Outline each blood parasite and name the species.
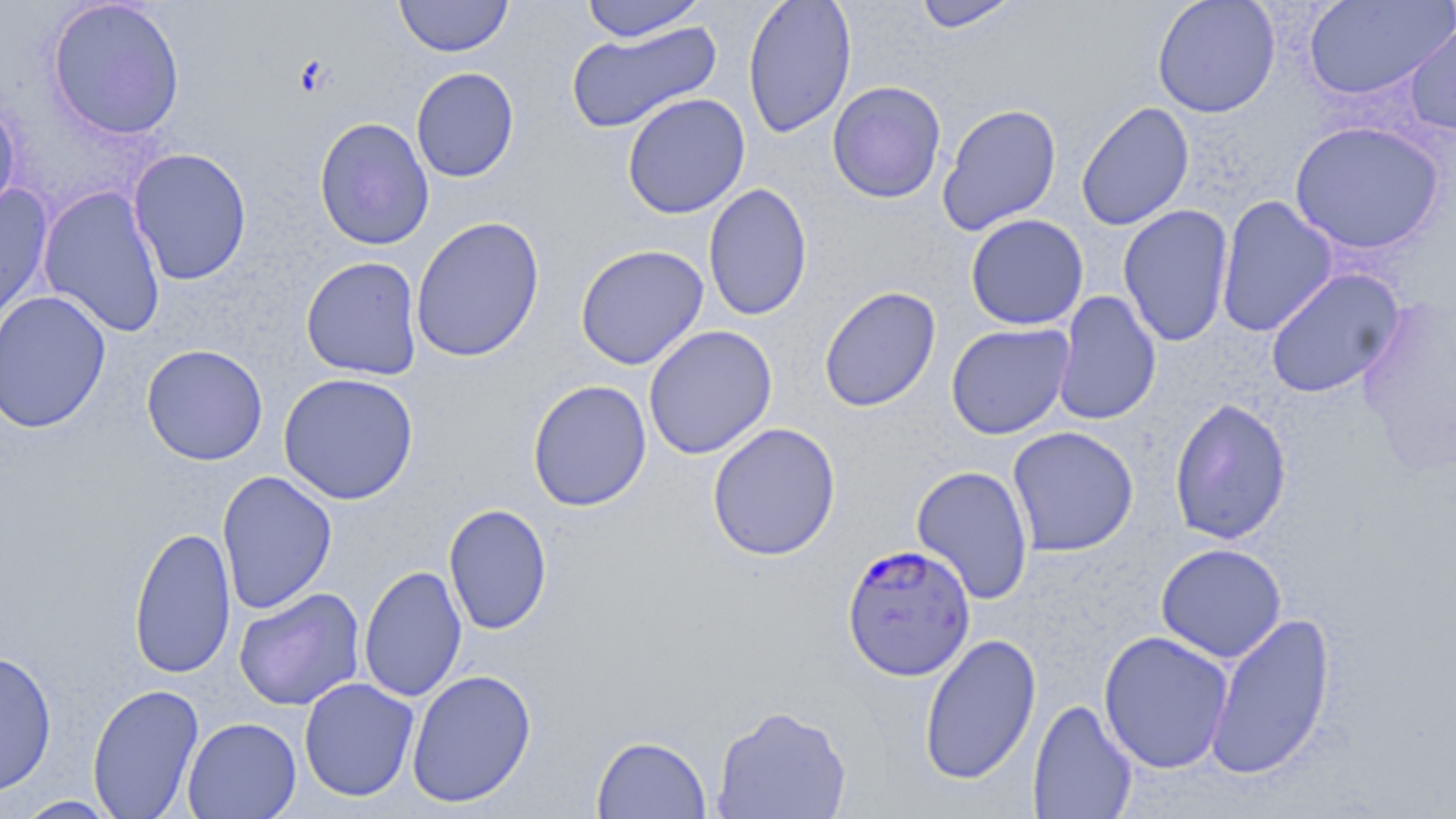
Approximate bounding boxes as [x1, y1, x2, y2] in pixels.
Plasmodium falciparum-infected red blood cells: [841, 542, 976, 683].
No Plasmodium ovale, Plasmodium malariae, Plasmodium vivax, Babesia divergens, or Trypanosoma brucei observed.

Uninfected red blood cell locations: [46, 0, 186, 140], [394, 0, 513, 57], [579, 0, 709, 42], [742, 0, 857, 139], [913, 0, 1020, 32], [1151, 0, 1280, 117], [1304, 0, 1455, 100], [566, 20, 722, 135], [1404, 20, 1456, 138], [411, 66, 520, 183], [826, 81, 946, 204], [0, 93, 21, 223], [622, 93, 750, 219], [1075, 101, 1195, 232], [937, 103, 1062, 236], [314, 117, 434, 251], [1289, 121, 1445, 255], [128, 147, 253, 285], [703, 182, 813, 322], [0, 186, 54, 335], [38, 186, 167, 338], [1215, 195, 1338, 338], [1117, 203, 1234, 347], [965, 213, 1089, 331], [411, 215, 546, 363], [575, 244, 709, 371], [301, 256, 423, 380], [1263, 268, 1406, 399], [818, 285, 942, 413], [0, 290, 112, 433], [1052, 291, 1162, 426], [1356, 295, 1456, 473], [945, 322, 1074, 440], [643, 325, 778, 460], [141, 344, 269, 466], [278, 372, 419, 505], [527, 379, 652, 512], [1169, 396, 1293, 545], [706, 421, 841, 561], [1006, 426, 1139, 557], [910, 465, 1035, 604], [217, 470, 338, 615], [443, 503, 552, 635], [128, 526, 237, 680], [1155, 543, 1287, 663], [359, 564, 466, 702], [234, 588, 366, 711], [1204, 611, 1337, 782], [1098, 630, 1234, 774], [919, 632, 1041, 785], [0, 647, 58, 798], [406, 669, 537, 809], [298, 677, 420, 801], [87, 683, 205, 818], [1027, 699, 1138, 818], [711, 704, 852, 819], [182, 717, 302, 818], [591, 734, 712, 818], [12, 795, 124, 818]. Slide-level diagnosis: Plasmodium falciparum. Optical microscopy. 1000x magnification. May-Grünwald-Giemsa stain. Image is 1456×819 pixels. Thin blood smear. One field of a larger specimen.